State which parasite is depicted.
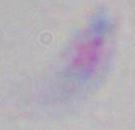

Toxoplasma gondii.

{
  "magnification": "1000x",
  "modality": "photomicrograph"
}